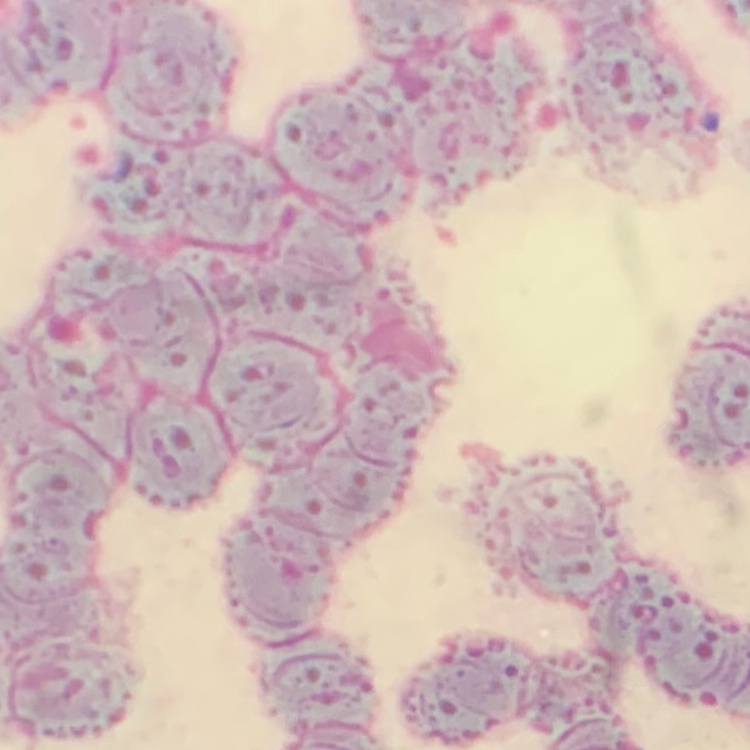

The erythrocytes show rouleaux formation. Thin blood film. Square crop of a larger photomicrograph. Stained with either Field's or Giemsa.